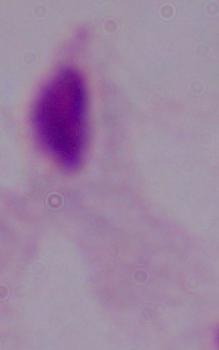

Summary:
  - Magnification: 1000x
  - Identification: trichomonad
  - Modality: photomicrograph